State which parasite is depicted.
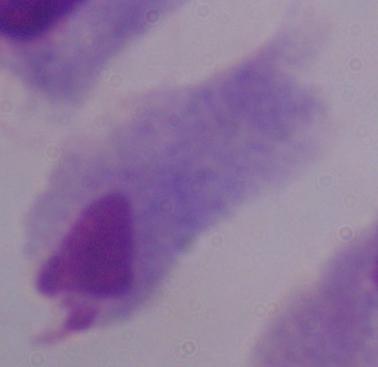
This is a trichomonad.

Summary:
  - Modality: photomicrograph
  - Magnification: 1000x